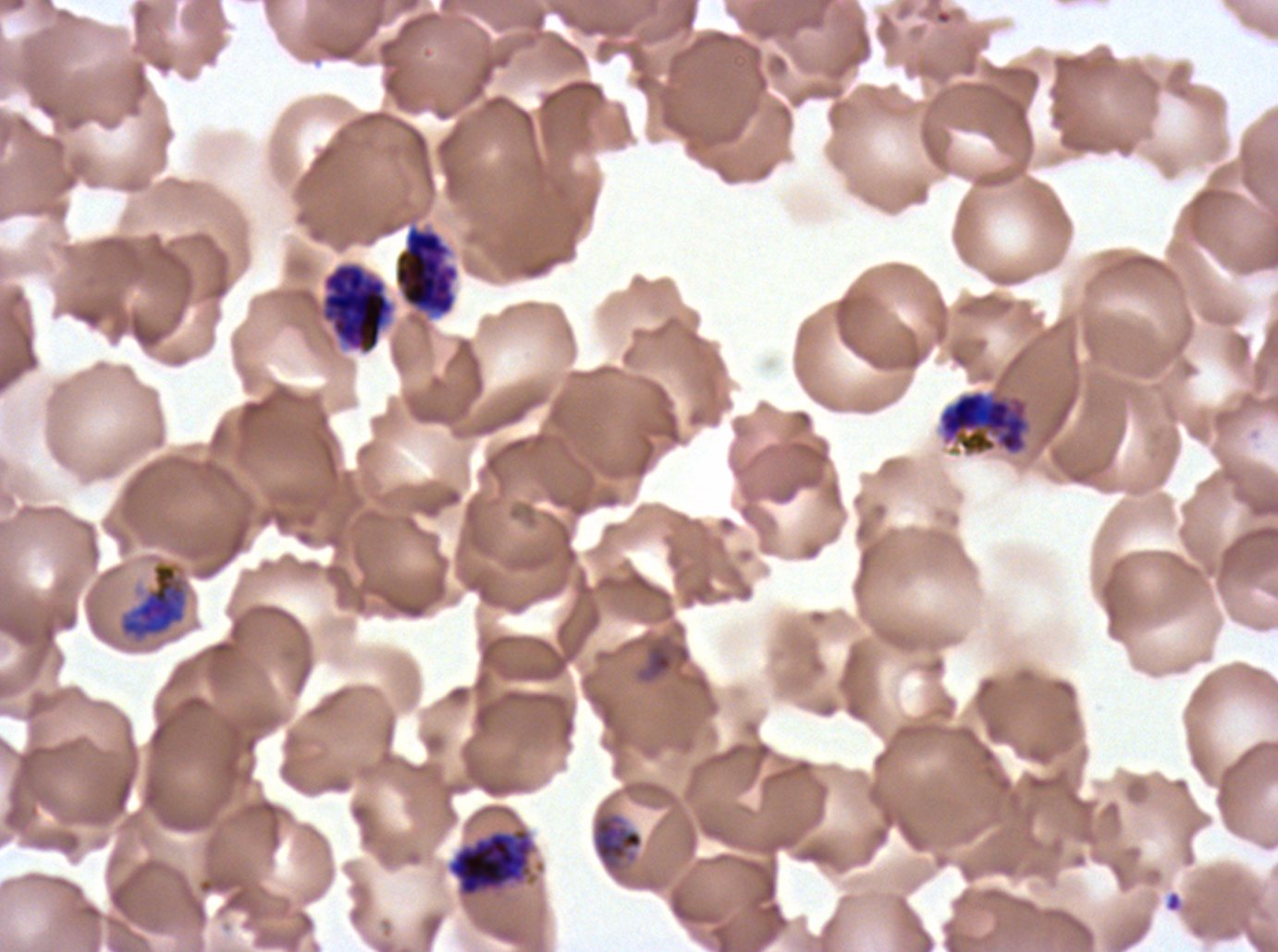
Approximate bounding boxes as {x1, y1, x2, y2} in pixels. Late trophozoite locations: {591, 812, 644, 871}. Late schizont locations: {393, 223, 461, 320}, {320, 261, 396, 356}, {447, 827, 535, 898}. Early schizont locations: {938, 389, 1032, 457}, {120, 563, 186, 639}. Debris locations: {1164, 890, 1184, 913}. Late-ring/early-trophozoite locations: {634, 634, 692, 685}. Thin blood smear. Life-cycle stages observed: late-ring/early-trophozoite, late trophozoite, early schizont, late schizont. Image is 1278×952 pixels. One sub-image of a larger composite. Giemsa stain. Plasmodium falciparum cultured ex vivo for 24 to 48 hours, from a patient in The Gambia.